State which cell type is depicted.
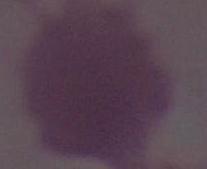

An erythrocyte.

Summary:
  - Magnification: 1000x
  - Modality: micrograph